Identify the blood parasite species.
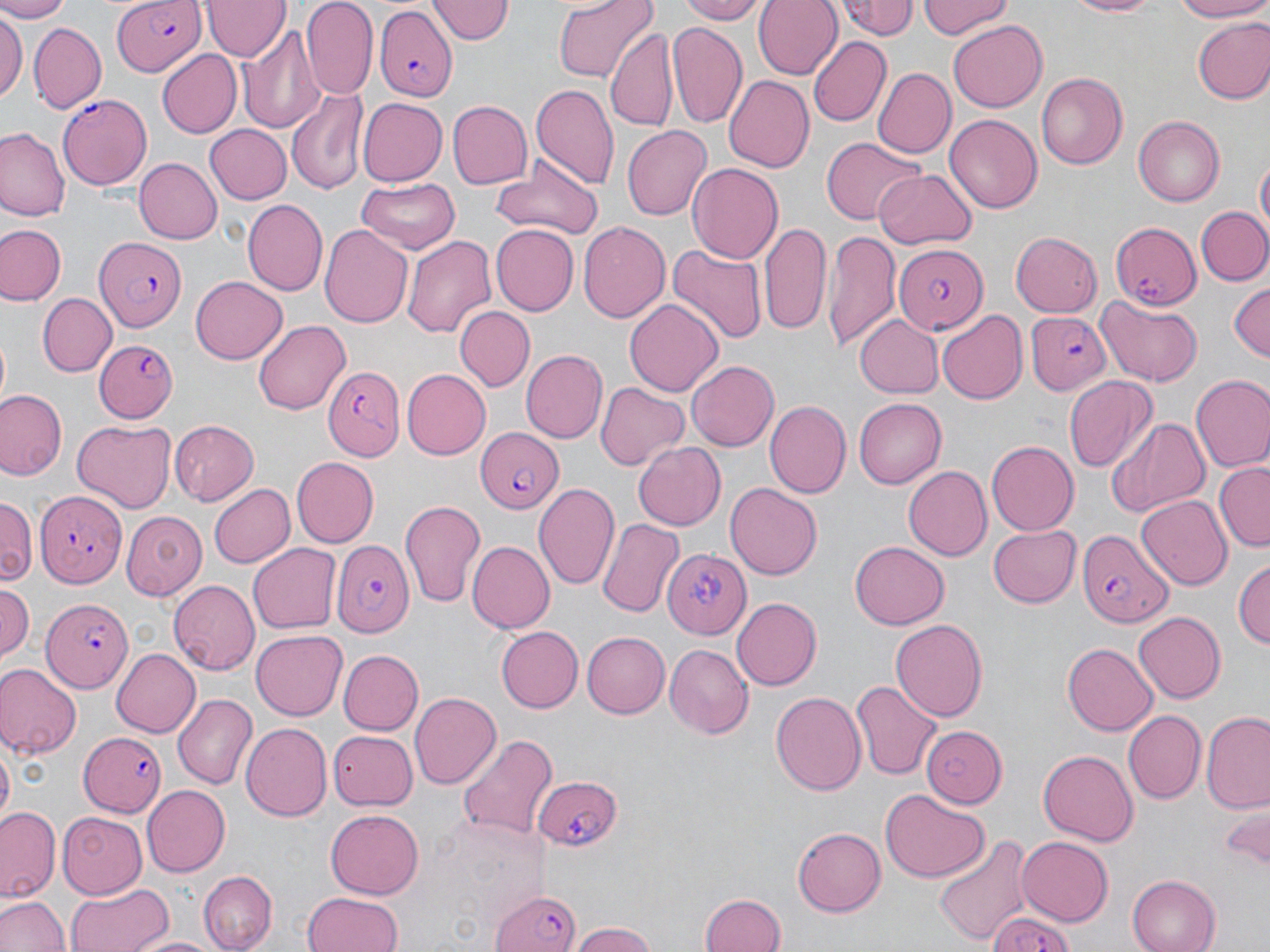
Plasmodium falciparum.

Approximate bounding boxes as named x1/y1/x2/y2 corners in pixels. Uninfected red blood cell locations: (x1=0, y1=0, x2=70, y2=21), (x1=202, y1=0, x2=288, y2=61), (x1=429, y1=0, x2=510, y2=45), (x1=552, y1=0, x2=656, y2=83), (x1=678, y1=0, x2=768, y2=23), (x1=754, y1=0, x2=844, y2=79), (x1=834, y1=0, x2=921, y2=43), (x1=917, y1=0, x2=1014, y2=39), (x1=1065, y1=0, x2=1167, y2=17), (x1=1170, y1=0, x2=1270, y2=22), (x1=302, y1=1, x2=377, y2=98), (x1=0, y1=11, x2=25, y2=108), (x1=1190, y1=17, x2=1270, y2=104), (x1=667, y1=20, x2=750, y2=132), (x1=949, y1=22, x2=1047, y2=112), (x1=28, y1=23, x2=105, y2=113), (x1=240, y1=25, x2=324, y2=134), (x1=607, y1=29, x2=675, y2=129), (x1=807, y1=36, x2=890, y2=126), (x1=154, y1=49, x2=241, y2=139), (x1=871, y1=66, x2=955, y2=158), (x1=1037, y1=71, x2=1128, y2=169), (x1=723, y1=75, x2=814, y2=174), (x1=531, y1=81, x2=620, y2=192), (x1=286, y1=87, x2=368, y2=194), (x1=357, y1=96, x2=446, y2=184), (x1=447, y1=101, x2=532, y2=188), (x1=945, y1=112, x2=1043, y2=213), (x1=1133, y1=115, x2=1226, y2=206), (x1=204, y1=125, x2=291, y2=204), (x1=622, y1=127, x2=711, y2=220), (x1=0, y1=128, x2=67, y2=221), (x1=821, y1=137, x2=926, y2=225), (x1=1255, y1=156, x2=1269, y2=238), (x1=136, y1=157, x2=222, y2=243), (x1=486, y1=163, x2=605, y2=240), (x1=687, y1=163, x2=784, y2=264), (x1=875, y1=167, x2=976, y2=248), (x1=354, y1=179, x2=460, y2=253), (x1=243, y1=200, x2=328, y2=296), (x1=1196, y1=205, x2=1270, y2=287), (x1=578, y1=221, x2=672, y2=324), (x1=759, y1=222, x2=830, y2=335), (x1=321, y1=223, x2=415, y2=329), (x1=1, y1=224, x2=64, y2=305), (x1=489, y1=224, x2=577, y2=314), (x1=1011, y1=230, x2=1103, y2=316), (x1=822, y1=231, x2=900, y2=350), (x1=401, y1=235, x2=496, y2=338), (x1=665, y1=242, x2=769, y2=344), (x1=190, y1=277, x2=288, y2=364), (x1=1227, y1=282, x2=1269, y2=362), (x1=39, y1=294, x2=113, y2=375), (x1=1095, y1=296, x2=1205, y2=386), (x1=625, y1=299, x2=723, y2=396), (x1=455, y1=306, x2=533, y2=392), (x1=938, y1=311, x2=1029, y2=404), (x1=853, y1=315, x2=943, y2=397), (x1=253, y1=320, x2=351, y2=415), (x1=520, y1=349, x2=607, y2=443), (x1=687, y1=359, x2=779, y2=453), (x1=402, y1=370, x2=490, y2=459), (x1=1192, y1=375, x2=1270, y2=474), (x1=1063, y1=377, x2=1159, y2=474), (x1=594, y1=382, x2=689, y2=470), (x1=0, y1=388, x2=66, y2=481), (x1=852, y1=398, x2=944, y2=488), (x1=764, y1=401, x2=850, y2=498), (x1=1104, y1=417, x2=1209, y2=516), (x1=71, y1=420, x2=176, y2=512), (x1=168, y1=420, x2=259, y2=505), (x1=987, y1=440, x2=1080, y2=535), (x1=631, y1=442, x2=726, y2=532), (x1=293, y1=457, x2=378, y2=547), (x1=1214, y1=464, x2=1269, y2=552), (x1=902, y1=466, x2=992, y2=560), (x1=209, y1=482, x2=295, y2=568), (x1=534, y1=483, x2=621, y2=592), (x1=725, y1=483, x2=821, y2=581), (x1=1137, y1=494, x2=1232, y2=588), (x1=0, y1=495, x2=36, y2=588), (x1=399, y1=498, x2=487, y2=606), (x1=543, y1=499, x2=675, y2=605), (x1=122, y1=509, x2=207, y2=595), (x1=597, y1=519, x2=685, y2=620), (x1=989, y1=524, x2=1082, y2=608), (x1=850, y1=539, x2=948, y2=627), (x1=469, y1=541, x2=554, y2=632), (x1=250, y1=545, x2=340, y2=631), (x1=1233, y1=555, x2=1270, y2=654), (x1=169, y1=581, x2=261, y2=675), (x1=0, y1=583, x2=35, y2=664), (x1=732, y1=597, x2=821, y2=690), (x1=1134, y1=611, x2=1226, y2=704), (x1=890, y1=618, x2=989, y2=721), (x1=497, y1=627, x2=584, y2=711), (x1=251, y1=630, x2=345, y2=719), (x1=581, y1=630, x2=670, y2=718), (x1=1064, y1=642, x2=1158, y2=734), (x1=664, y1=645, x2=751, y2=738), (x1=110, y1=647, x2=200, y2=738), (x1=336, y1=649, x2=421, y2=735), (x1=0, y1=663, x2=79, y2=759), (x1=852, y1=680, x2=942, y2=778), (x1=770, y1=690, x2=866, y2=797), (x1=409, y1=692, x2=500, y2=790), (x1=172, y1=693, x2=256, y2=790), (x1=1201, y1=709, x2=1270, y2=816), (x1=1123, y1=710, x2=1206, y2=805), (x1=243, y1=723, x2=334, y2=820), (x1=918, y1=724, x2=1007, y2=807), (x1=328, y1=730, x2=417, y2=810), (x1=456, y1=732, x2=558, y2=843), (x1=0, y1=744, x2=13, y2=832), (x1=1037, y1=747, x2=1138, y2=846), (x1=141, y1=786, x2=229, y2=876), (x1=881, y1=789, x2=984, y2=882), (x1=2, y1=806, x2=61, y2=902), (x1=1219, y1=806, x2=1268, y2=866), (x1=325, y1=807, x2=423, y2=896), (x1=58, y1=810, x2=146, y2=895), (x1=793, y1=828, x2=885, y2=915), (x1=933, y1=835, x2=1034, y2=947), (x1=1016, y1=836, x2=1112, y2=926), (x1=200, y1=871, x2=276, y2=950), (x1=1126, y1=873, x2=1219, y2=952), (x1=65, y1=882, x2=171, y2=952), (x1=304, y1=892, x2=404, y2=952), (x1=699, y1=892, x2=788, y2=950), (x1=0, y1=894, x2=67, y2=952), (x1=566, y1=921, x2=662, y2=951), (x1=133, y1=935, x2=219, y2=952). Plasmodium falciparum-infected red blood cell locations: (x1=112, y1=1, x2=206, y2=75), (x1=375, y1=7, x2=457, y2=101), (x1=57, y1=92, x2=152, y2=187), (x1=1108, y1=219, x2=1199, y2=311), (x1=95, y1=236, x2=187, y2=333), (x1=896, y1=242, x2=990, y2=335), (x1=1025, y1=312, x2=1113, y2=395), (x1=93, y1=339, x2=177, y2=422), (x1=325, y1=366, x2=403, y2=461), (x1=473, y1=427, x2=562, y2=513), (x1=38, y1=492, x2=127, y2=586), (x1=1076, y1=528, x2=1170, y2=627), (x1=331, y1=537, x2=415, y2=633), (x1=663, y1=547, x2=753, y2=640), (x1=41, y1=598, x2=131, y2=693), (x1=79, y1=732, x2=166, y2=817), (x1=532, y1=774, x2=624, y2=851), (x1=489, y1=884, x2=585, y2=952), (x1=986, y1=909, x2=1083, y2=952). Captured at 1000x magnification. One field of a larger specimen. May-Grünwald-Giemsa stain. Optical microscopy. Thin blood film. Image is 1270×952 pixels.